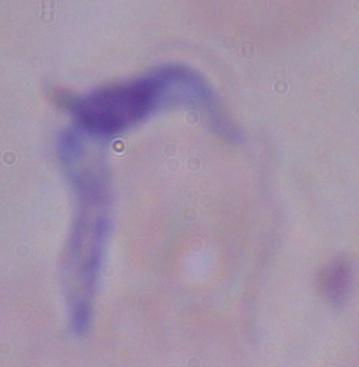

1000x magnification. Micrograph. A trypanosome is seen.